Give the position of every Plasmodium parasite.
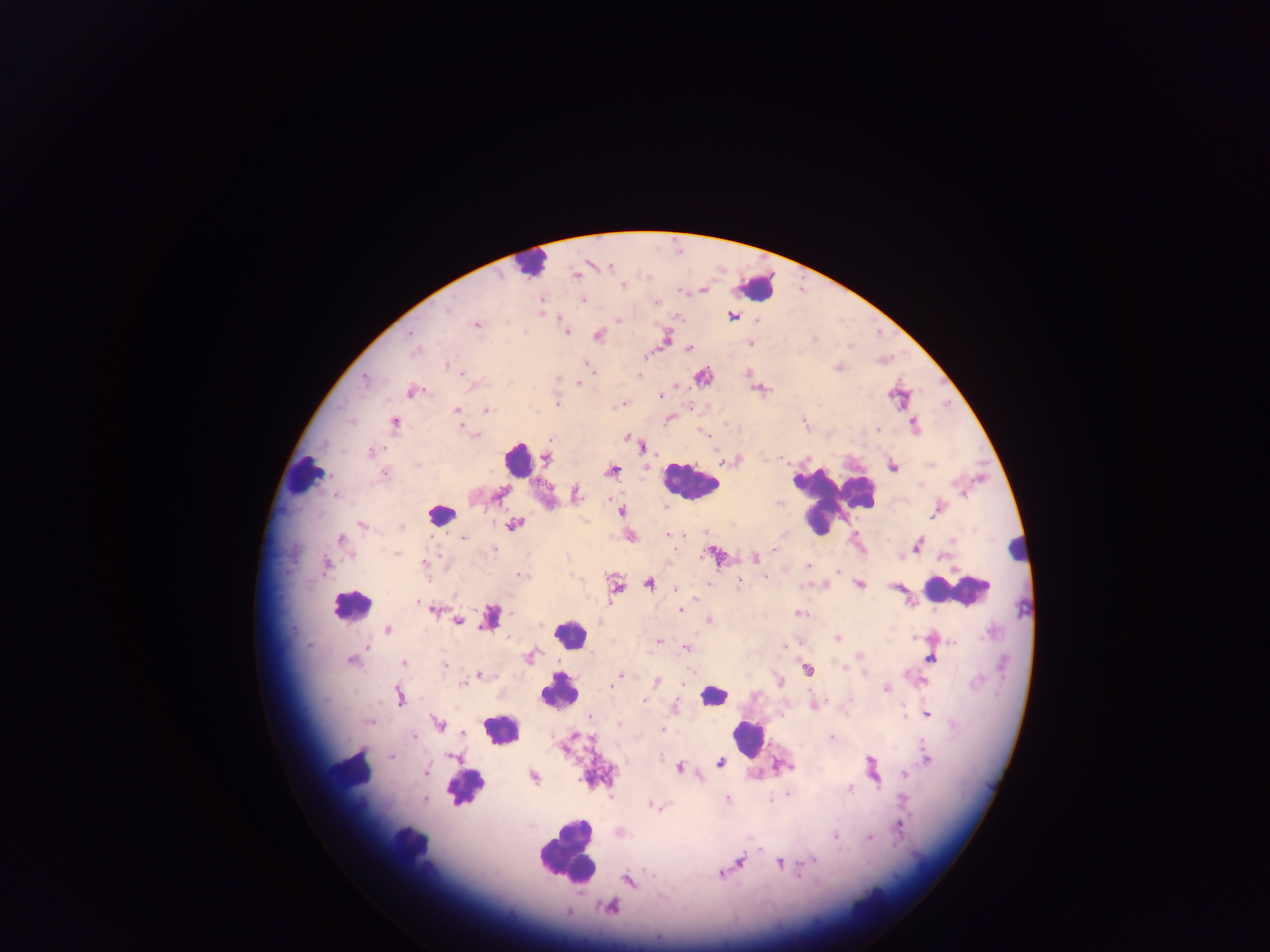
Approximate centers as [x, y] in pixels.
Plasmodium parasites: [575, 275], [623, 284], [702, 290], [582, 299], [540, 300], [655, 301], [541, 312], [732, 316], [616, 319], [758, 319], [476, 324], [565, 330], [409, 334], [598, 334], [666, 338], [750, 342], [688, 348], [584, 363], [448, 365], [749, 372], [638, 375], [702, 376], [364, 379], [578, 383], [759, 388], [411, 391], [660, 395], [899, 396], [558, 402], [622, 403], [455, 409], [486, 410], [669, 417], [393, 421], [805, 422], [914, 426], [465, 428], [877, 429], [474, 435], [628, 437], [642, 447], [371, 452], [546, 456], [733, 460], [726, 461], [892, 465], [646, 466], [611, 471], [384, 473], [499, 494], [575, 494], [335, 495], [938, 508], [621, 511], [513, 524], [362, 525], [401, 527], [668, 534], [463, 536], [629, 536], [340, 538], [917, 544], [775, 548], [396, 553], [714, 555], [900, 555], [755, 557], [423, 564], [325, 566], [808, 566], [839, 571], [521, 576], [707, 582], [739, 582], [649, 583], [859, 584], [614, 586], [895, 587], [677, 590], [417, 600], [434, 609], [680, 609], [798, 613], [709, 620], [457, 621], [387, 630], [837, 637], [659, 641], [783, 644], [366, 646], [687, 649], [530, 655], [932, 657], [351, 660], [403, 663], [444, 664], [807, 668], [863, 671], [479, 674], [619, 675], [778, 681], [656, 682], [462, 683], [613, 683], [886, 688], [398, 696], [645, 701], [814, 705], [674, 707], [926, 713], [590, 716], [438, 724], [619, 724], [662, 729], [462, 733], [413, 736], [831, 738], [392, 756], [453, 757], [926, 759], [721, 763], [783, 766], [679, 767], [871, 768], [425, 771], [904, 772], [533, 776], [850, 788], [424, 798], [727, 799], [652, 806], [900, 824], [619, 832], [835, 836], [869, 837], [812, 859], [740, 861], [781, 862], [721, 874], [628, 880], [610, 907].

Leukocyte locations: [529, 263], [756, 288], [539, 456], [517, 459], [304, 476], [689, 482], [836, 496], [441, 515], [1017, 547], [957, 590], [350, 606], [490, 617], [569, 633], [559, 690], [712, 695], [501, 729], [749, 740], [351, 770], [464, 788], [408, 844], [566, 852]. Single field of view. Photographed through a microscope with a mobile-phone camera. Image is 1270×952 pixels. Thick blood film. Sample from Ghana.